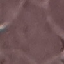

{
  "result": "no malaria parasites detected",
  "capture": "smartphone camera at the microscope eyepiece",
  "preparation": "thin blood smear",
  "image_type": "cell patch, automatically extracted from a larger field of view and resized to 64 × 64 pixels",
  "stain": "Giemsa"
}